Locate every blood parasite and identify its species.
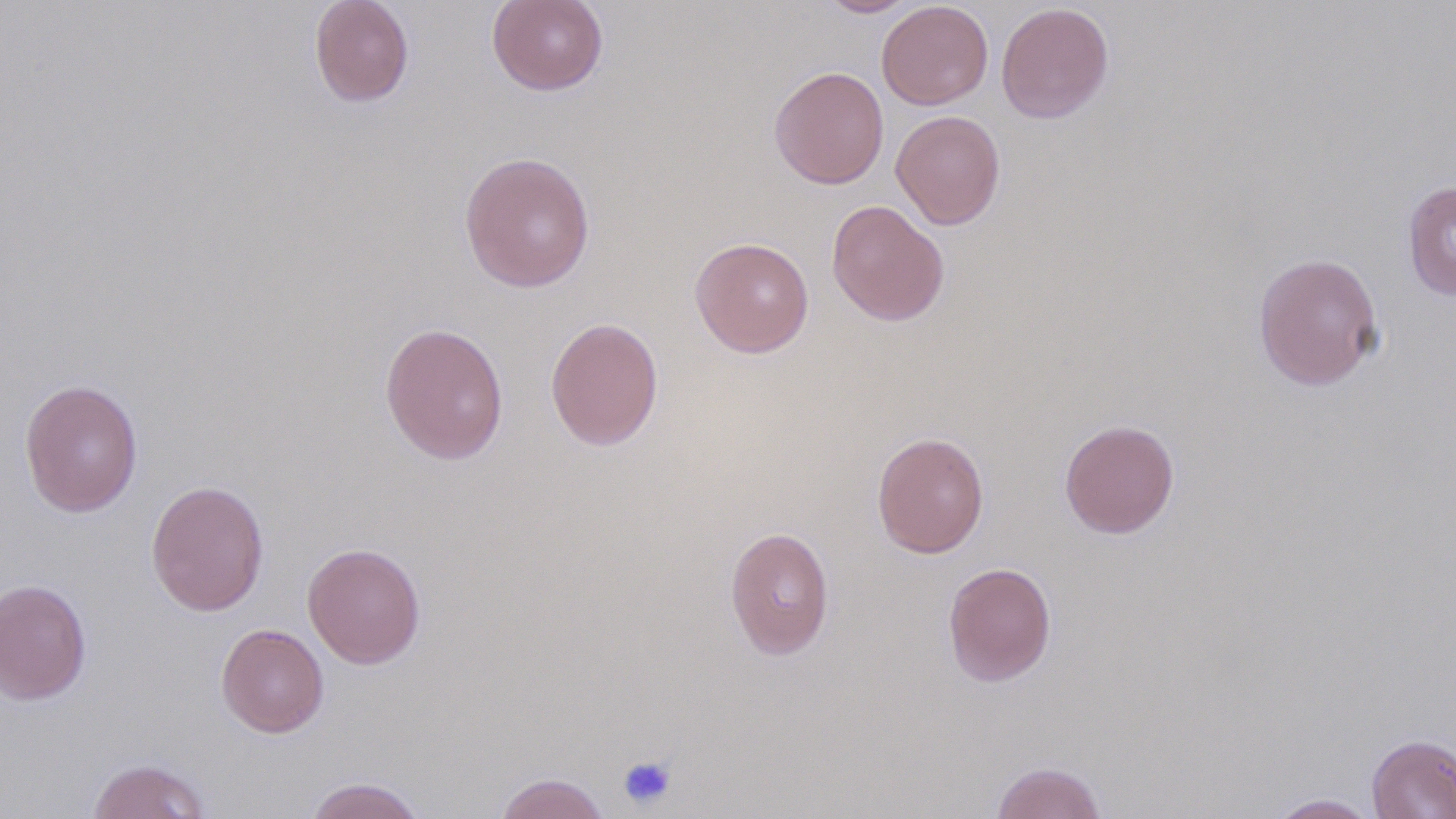
No blood parasites seen.

Approximate bounding boxes as (x1,y1)-(x2,y2) corner pairs in pixels. Platelet locations: (616,754)-(678,810). Uninfected red blood cell locations: (309,0)-(415,108), (487,0)-(609,96), (816,0)-(921,17), (877,1)-(993,110), (996,3)-(1114,123), (769,66)-(889,189), (891,110)-(1006,230), (458,151)-(596,293), (1401,179)-(1456,300), (826,199)-(950,327), (690,237)-(815,358), (1252,252)-(1384,391), (544,316)-(665,451), (379,321)-(509,465), (19,378)-(144,517), (1059,418)-(1180,539), (871,431)-(989,558), (145,479)-(270,617), (724,526)-(835,660), (302,542)-(426,669), (942,561)-(1057,686), (0,578)-(93,705), (216,623)-(329,738), (1366,733)-(1456,818), (85,757)-(212,818), (991,760)-(1107,819), (492,772)-(612,819), (303,776)-(428,819), (1268,793)-(1382,818). Slide-level diagnosis: negative for blood parasites. Image is 1456×819 pixels. One field of a larger specimen. May-Grünwald-Giemsa stain. Thin blood smear. Light microscopy. Captured at 1000x magnification.